Classify this cell by malaria status.
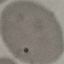
It is parasitized.

preparation: thin blood film
image_type: automatically extracted cell patch, resized to 64 × 64 pixels
capture: smartphone camera at the microscope eyepiece
stain: Giemsa